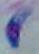
modality = photomicrograph
identification = Toxoplasma gondii
magnification = 1000x